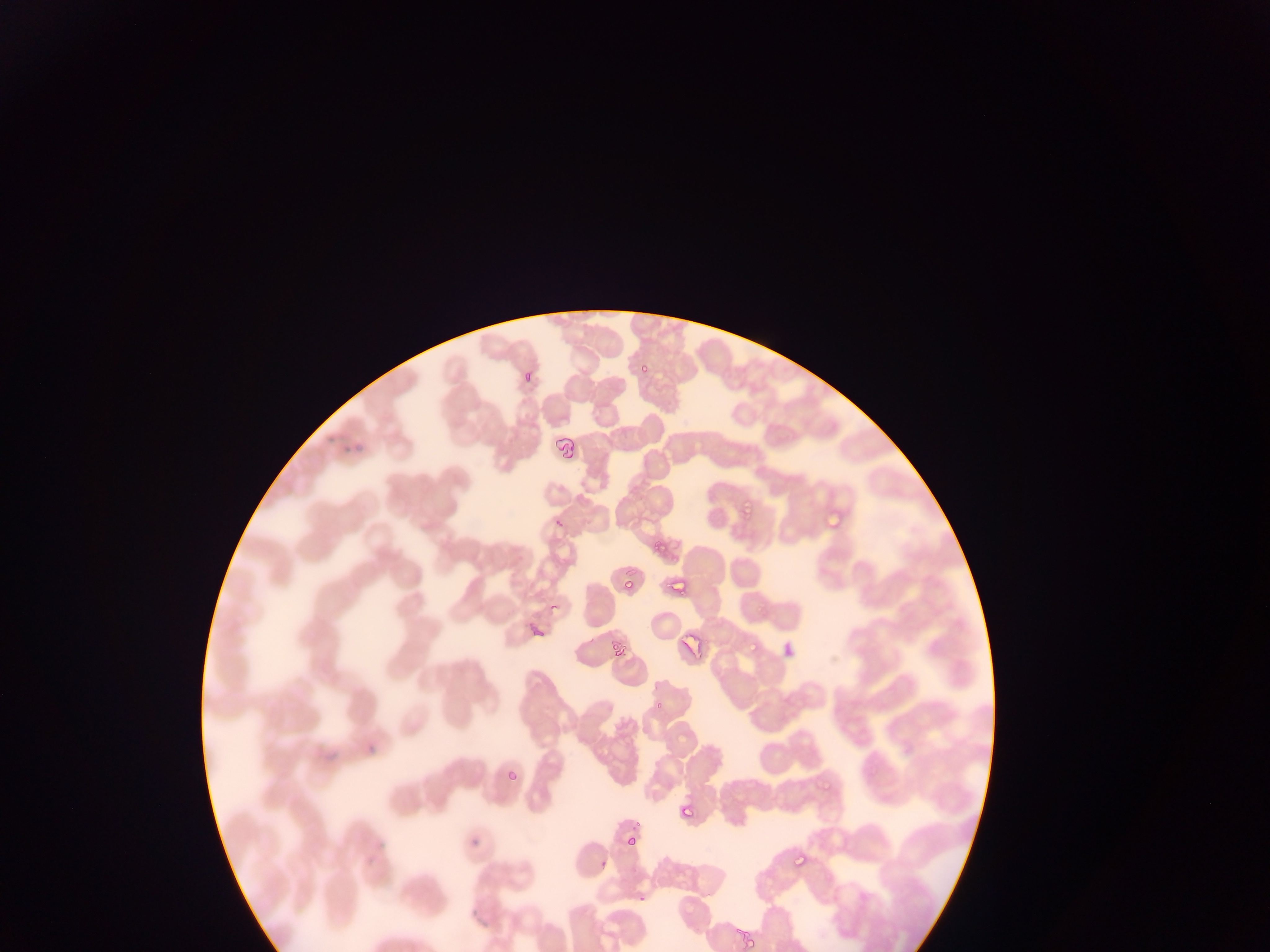
Approximate bounding boxes as [left, top, right, bottom] in pixels.
Summary:
  - Malaria parasite locations (subset; some below the resolvable size): [633, 364, 655, 381], [521, 368, 533, 384], [740, 481, 766, 529], [653, 538, 665, 555], [619, 575, 638, 591], [665, 575, 689, 590], [746, 631, 777, 656], [609, 640, 622, 656], [649, 700, 661, 713], [502, 760, 527, 784], [822, 778, 836, 793], [678, 803, 694, 819], [625, 832, 633, 847], [788, 855, 809, 872], [597, 856, 612, 870], [742, 935, 760, 952]
  - Field of view: single
  - Country: Ghana
  - Capture: mobile-phone photograph through a microscope
  - Preparation: thin blood smear
  - Image size: 1270×952 pixels